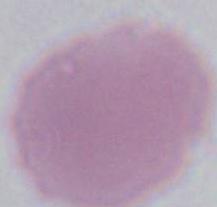

Summary:
  - Magnification: 1000x
  - Identification: red blood cell
  - Modality: photomicrograph